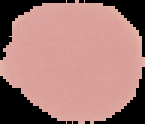

Summary:
  - Image size: 145×124 pixels
  - Preparation: thin blood smear
  - Malaria status: uninfected
  - Image type: segmented cell region on a black background